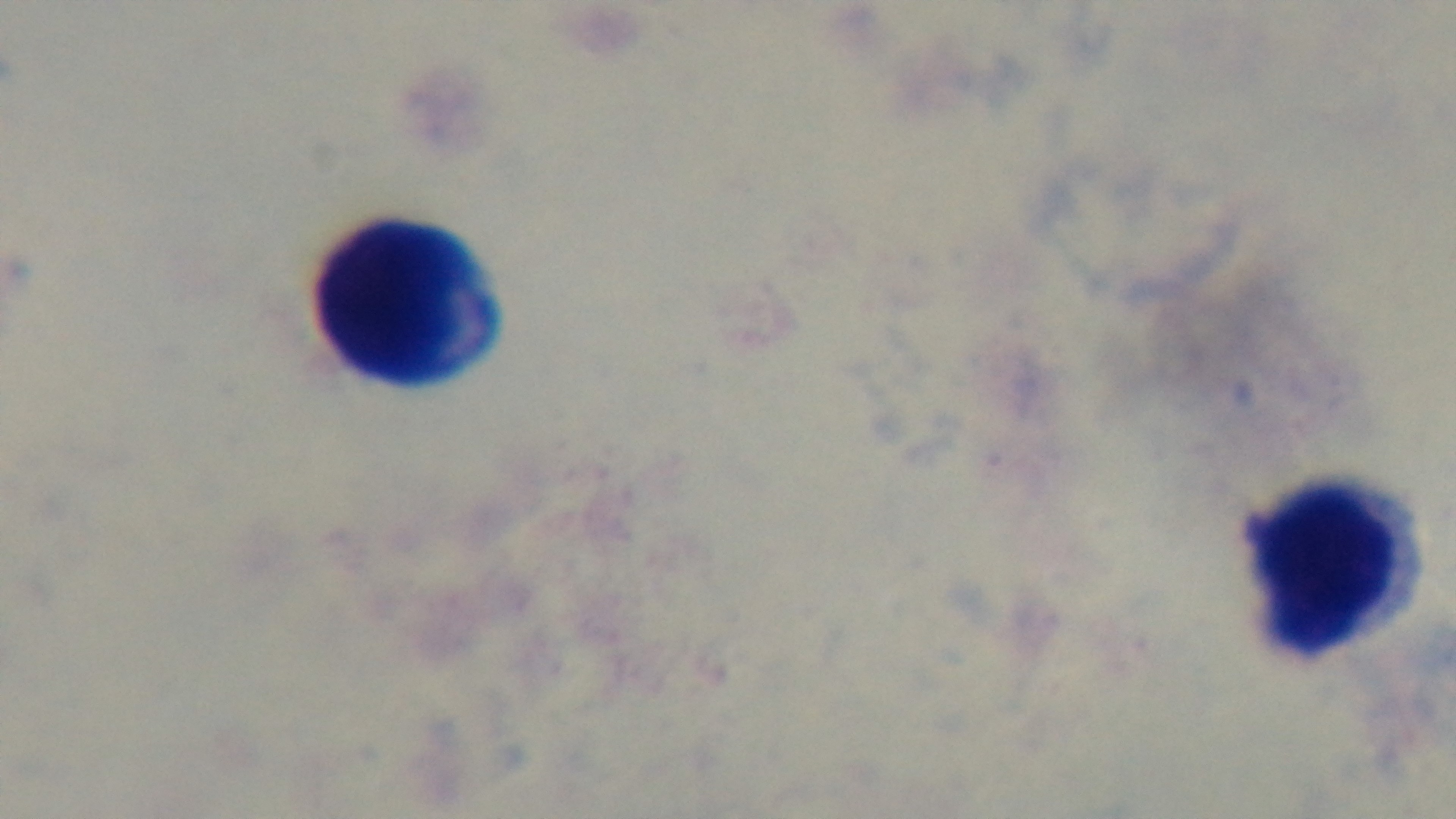

{
  "malaria_status": "uninfected",
  "objective": "100x oil immersion",
  "modality": "light microscopy",
  "preparation": "thick smear",
  "capture": "mounted 4K digital camera",
  "field_of_view": "one from the slide",
  "stain": "Giemsa"
}